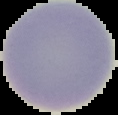

Segmented cell region on a black background. Malaria status: uninfected. Image is 118×115 pixels. From a thin blood film.